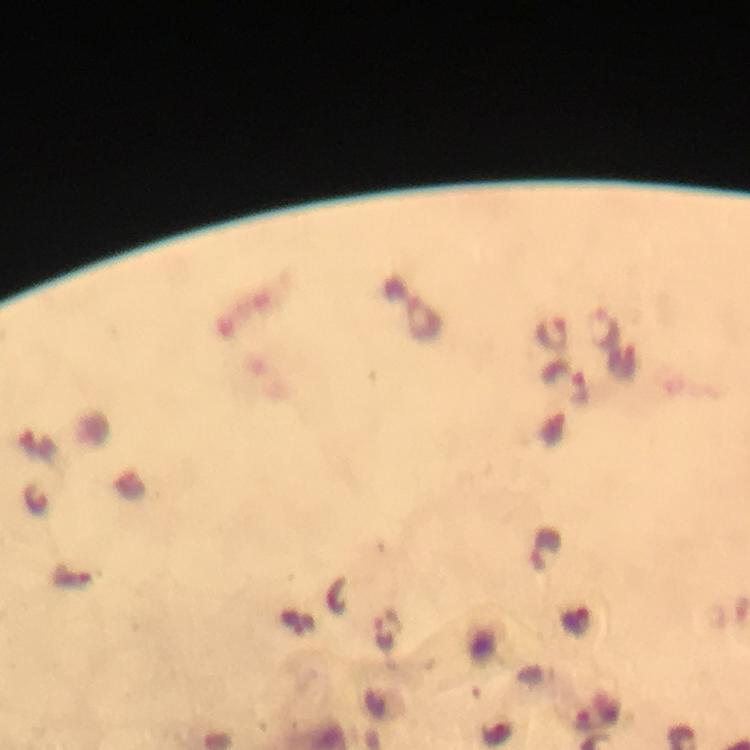

Approximate centers as [x, y] in pixels. Plasmodium parasite locations: [423, 317], [605, 329], [553, 332], [623, 363], [565, 383], [37, 499], [546, 543], [72, 575], [578, 621], [386, 630], [494, 731]. From a diagnostic examination for malaria. Giemsa-stained preparation. Image is 750×750 pixels. At 100x magnification. A crop from one field of view. Photographed through the microscope with a smartphone camera. Immersion oil applied. Thick blood film.